Comment on the morphology of the red blood cells.
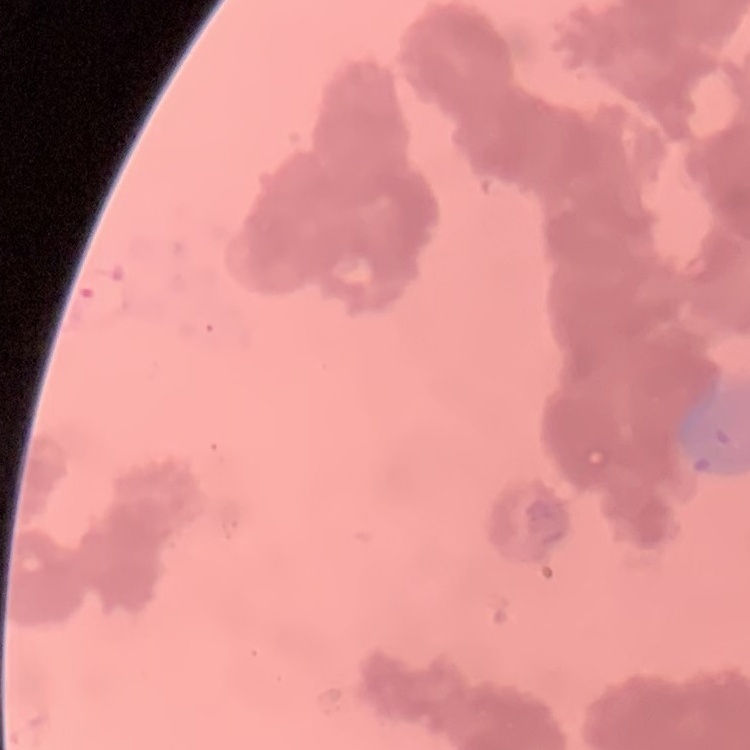
Rouleaux formation.

stain = Field's or Giemsa
image type = one tile cut from a larger photomicrograph
preparation = thin blood film